Comment on the morphology of the red blood cells.
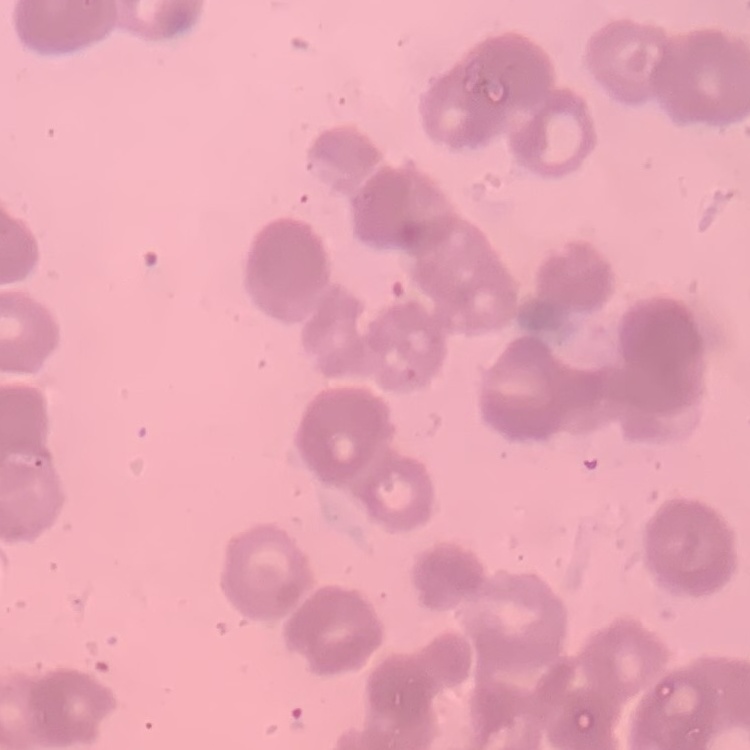

They show rouleaux formation.

preparation = thin peripheral smear
image type = one tile cut from a larger photomicrograph
stain = Field's or Giemsa